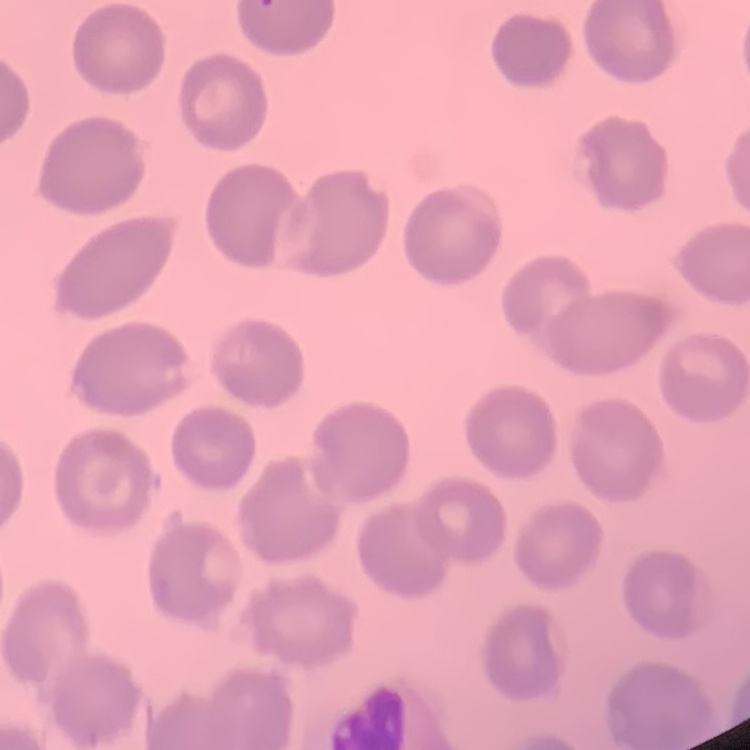
Summary:
  - Erythrocyte morphology: no rouleaux formation
  - Preparation: thin peripheral smear
  - Image type: square crop of a larger photomicrograph
  - Stain: Field's or Giemsa